Classify this cell by malaria status.
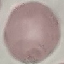
It is uninfected.

preparation = thin blood smear
image type = cell patch, automatically extracted from a larger field of view and resized to 64 × 64 pixels
capture = smartphone through the microscope eyepiece
stain = Giemsa